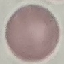
Summary:
  - Result: no malaria parasites detected
  - Image type: automatically extracted cell patch, resized to 64 × 64 pixels
  - Preparation: thin blood smear
  - Stain: Giemsa
  - Capture: smartphone through the microscope eyepiece